State the blood parasite species.
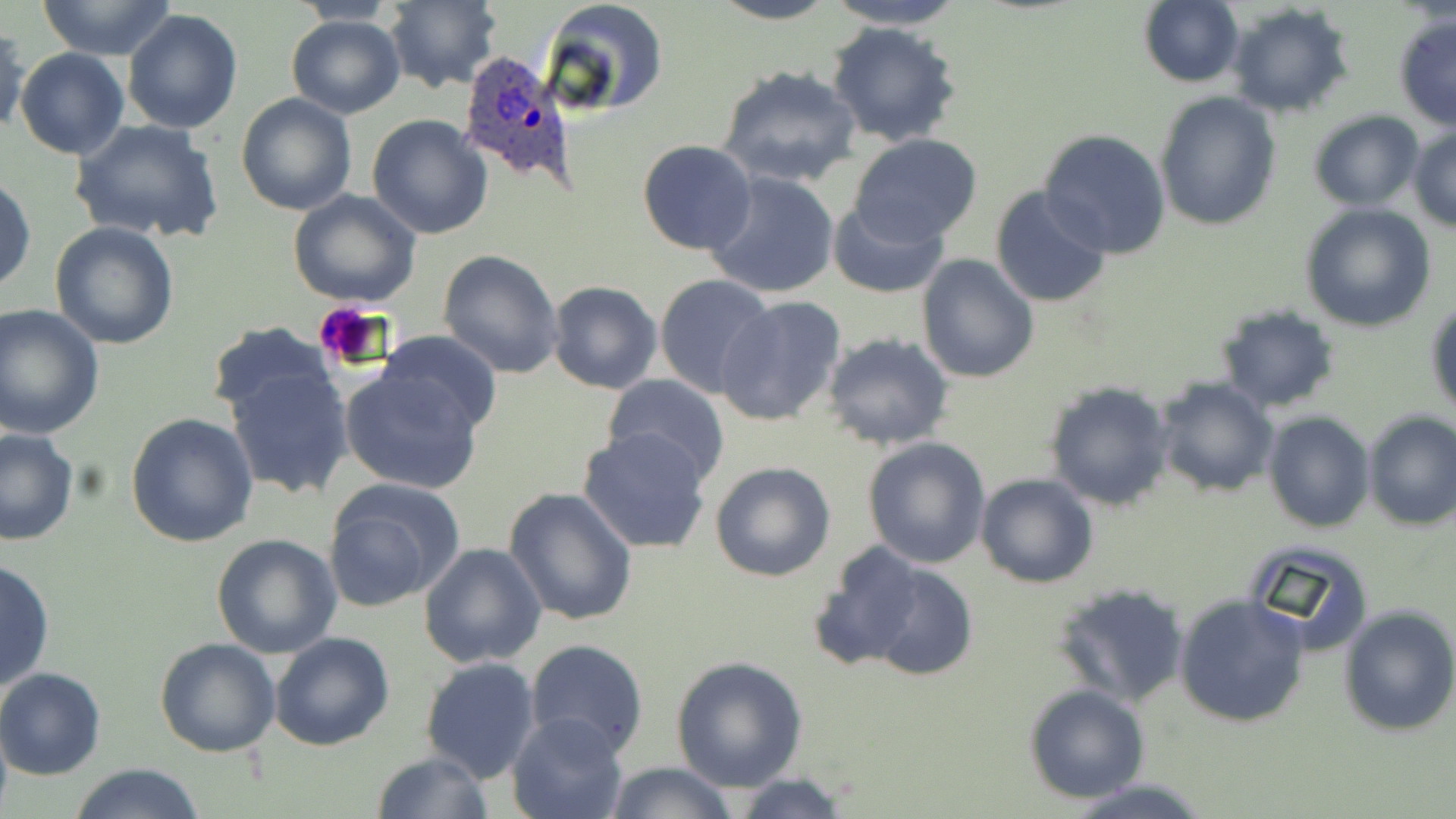
Plasmodium ovale.

Summary:
  - Coordinate format: approximate bounding boxes as [x1, y1, x2, y2] in pixels
  - Plasmodium ovale-infected red blood cell locations: [454, 51, 578, 185]
  - Platelet locations: [312, 301, 395, 374]
  - Uninfected red blood cell locations: [35, 0, 178, 60], [383, 0, 501, 92], [541, 0, 668, 117], [711, 0, 839, 25], [822, 0, 970, 30], [1137, 0, 1245, 88], [288, 1, 405, 26], [1226, 3, 1356, 119], [123, 8, 243, 133], [286, 14, 405, 118], [1393, 15, 1455, 130], [826, 21, 962, 148], [1, 24, 29, 138], [16, 47, 129, 160], [718, 64, 859, 188], [234, 92, 358, 217], [1155, 93, 1281, 230], [1308, 111, 1426, 210], [367, 114, 494, 240], [68, 117, 228, 245], [1408, 125, 1456, 233], [1039, 128, 1171, 259], [849, 133, 984, 244], [638, 140, 759, 255], [1, 171, 36, 296], [705, 171, 840, 300], [988, 184, 1113, 311], [286, 190, 424, 310], [827, 198, 947, 298], [1298, 202, 1436, 333], [49, 222, 180, 351], [437, 248, 565, 378], [915, 255, 1040, 383], [653, 272, 777, 398], [546, 281, 663, 394], [715, 295, 848, 428], [1426, 301, 1456, 417], [0, 305, 104, 440], [1215, 306, 1339, 413], [205, 323, 335, 422], [379, 330, 503, 437], [823, 333, 954, 450], [221, 358, 356, 500], [339, 365, 485, 494], [602, 375, 731, 487], [1151, 376, 1279, 498], [1043, 380, 1175, 511], [1362, 410, 1456, 530], [125, 411, 259, 547], [1263, 411, 1374, 533], [0, 427, 78, 545], [579, 427, 712, 554], [862, 436, 992, 569], [710, 461, 837, 583], [975, 473, 1100, 588], [322, 477, 466, 611], [502, 488, 638, 629], [211, 534, 343, 660], [1241, 540, 1374, 658], [809, 542, 930, 670], [419, 543, 547, 667], [846, 555, 979, 683], [0, 557, 55, 696], [1050, 581, 1188, 709], [1173, 592, 1313, 728], [1338, 605, 1456, 737], [269, 631, 395, 751], [153, 637, 282, 757], [524, 638, 649, 757], [420, 656, 540, 784], [671, 657, 808, 791], [0, 668, 106, 779], [1023, 683, 1151, 804], [507, 712, 630, 819], [370, 749, 494, 819], [66, 762, 208, 819], [604, 762, 738, 819], [727, 774, 856, 818], [1067, 778, 1213, 818]
  - Modality: optical microscopy
  - Magnification: 1000x
  - Image size: 1456×819 pixels
  - Field of view: one of a larger specimen
  - Preparation: thin blood smear
  - Stain: May-Grünwald-Giemsa